Describe the morphology of the red blood cells.
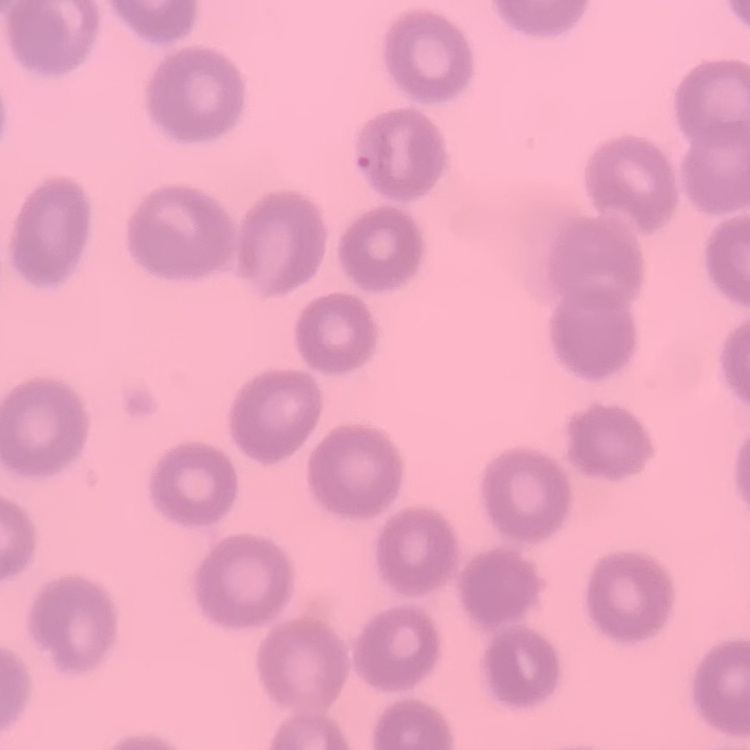

They show no rouleaux formation.

Summary:
  - Preparation: thin blood film
  - Image type: square crop of a larger photomicrograph
  - Stain: Field's or Giemsa